Name the parasite shown.
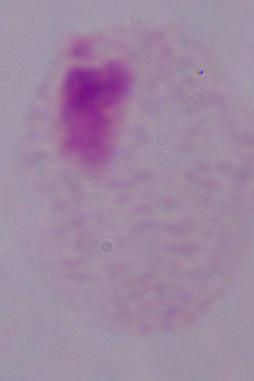

A trichomonad.

1000x magnification. Photomicrograph.